Assess the background quality.
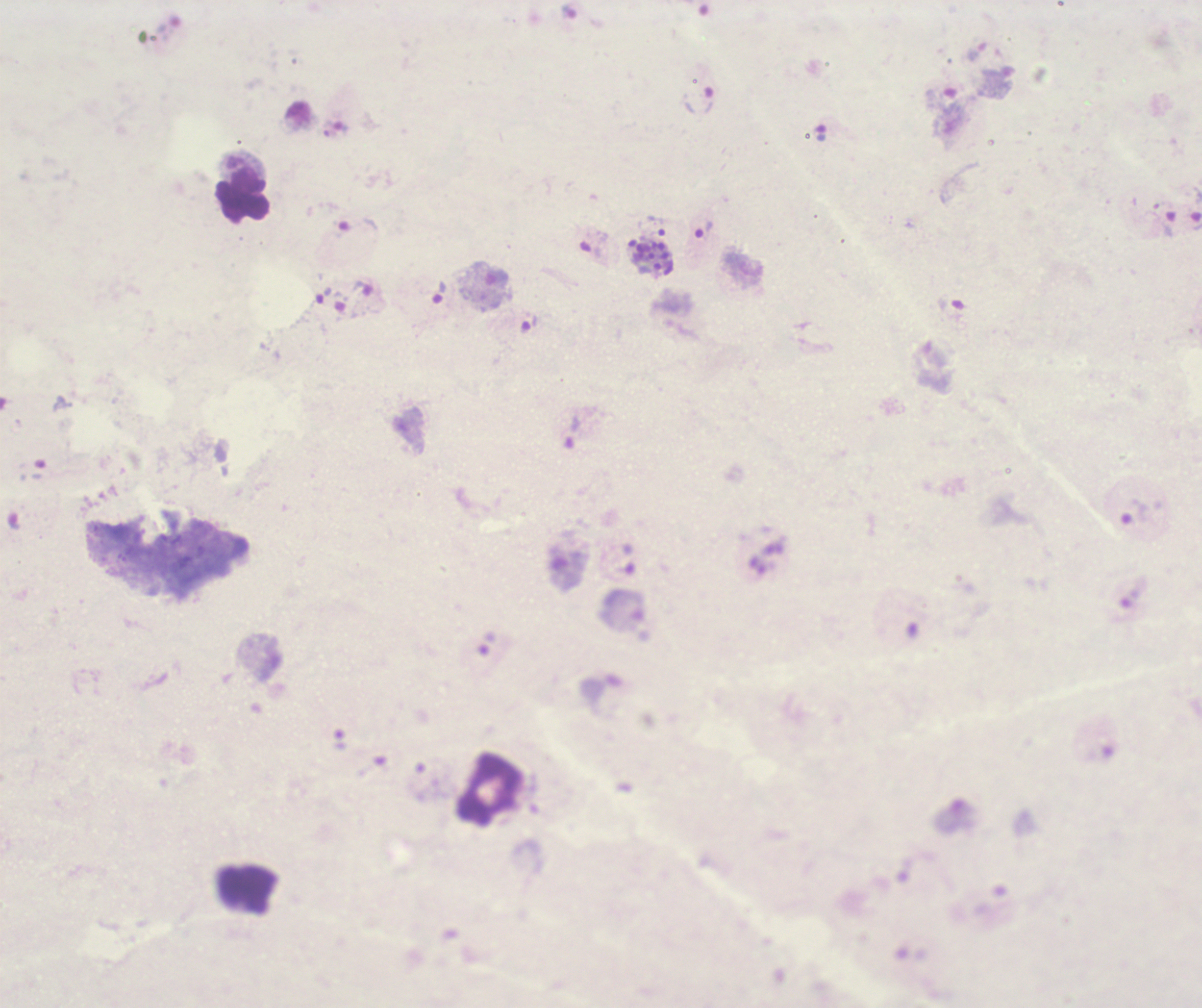

Poor.

coordinate format = approximate object centers, in pixels from the top-left corner
trophozoite locations = (x=698, y=100), (x=1161, y=222), (x=657, y=225), (x=704, y=230), (x=439, y=292)
leukocyte locations = (x=245, y=196), (x=489, y=790)
schizont locations = (x=651, y=256)
life-cycle stages observed = trophozoite, schizont
magnification = 100x
preparation = thick smear of blood
result = positive for Plasmodium parasites
image size = 1202×1008 pixels
coloration quality = bad
field of view = one from this slide
stain = Romanowsky
context = previously used in a real diagnosis